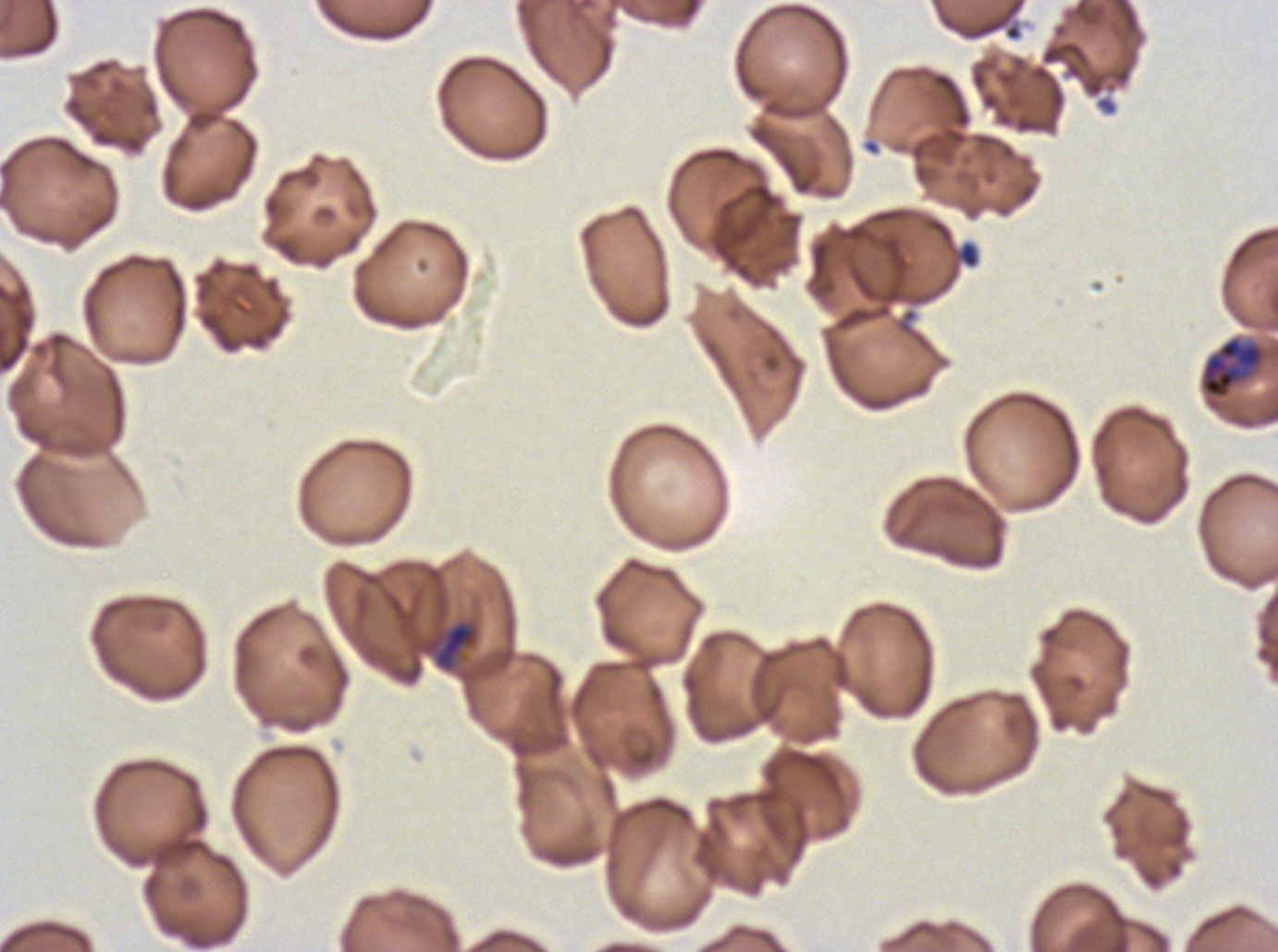

notation = approximate bounding rectangles given as corner coordinates in pixels from the top-left
debris locations = (x1=1004, y1=25, x2=1021, y2=41), (x1=960, y1=243, x2=978, y2=268)
late trophozoite locations = (x1=1198, y1=335, x2=1268, y2=400), (x1=434, y1=621, x2=478, y2=673)
field of view = one sub-image of a larger composite
preparation = thin blood smear
image size = 1278×952 pixels
specimen = Plasmodium falciparum cultured ex vivo for 24 to 48 hours, from a patient in The Gambia
stain = Giemsa